Comment on the morphology of the erythrocytes.
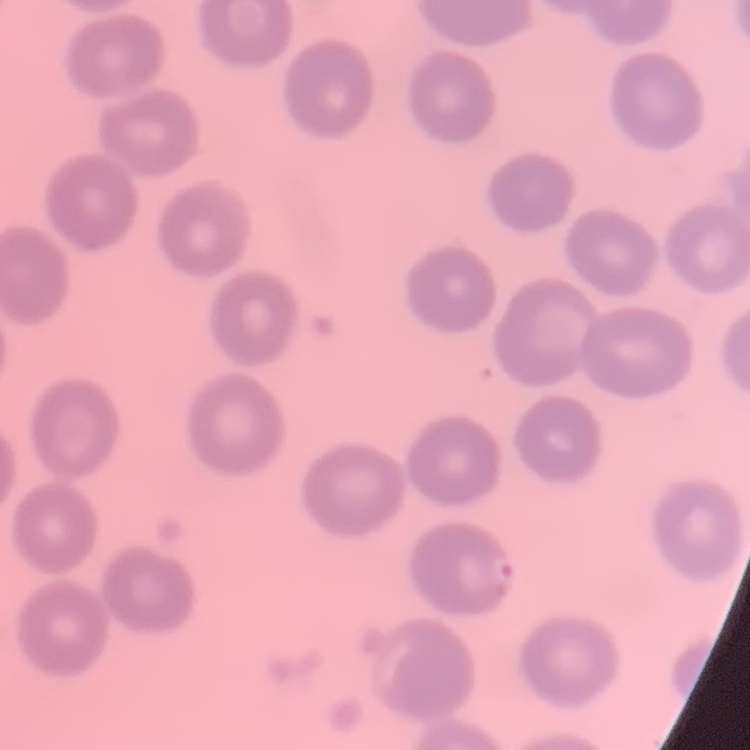

No rouleaux formation.

Stained with either Field's or Giemsa. Thin blood smear. Square crop of a larger photomicrograph.